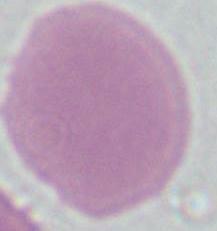
A red blood cell is shown. 1000x magnification. Photomicrograph.